Name the parasite shown.
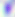
Toxoplasma gondii.

modality: photomicrograph
magnification: 400x